Identify the blood parasite species.
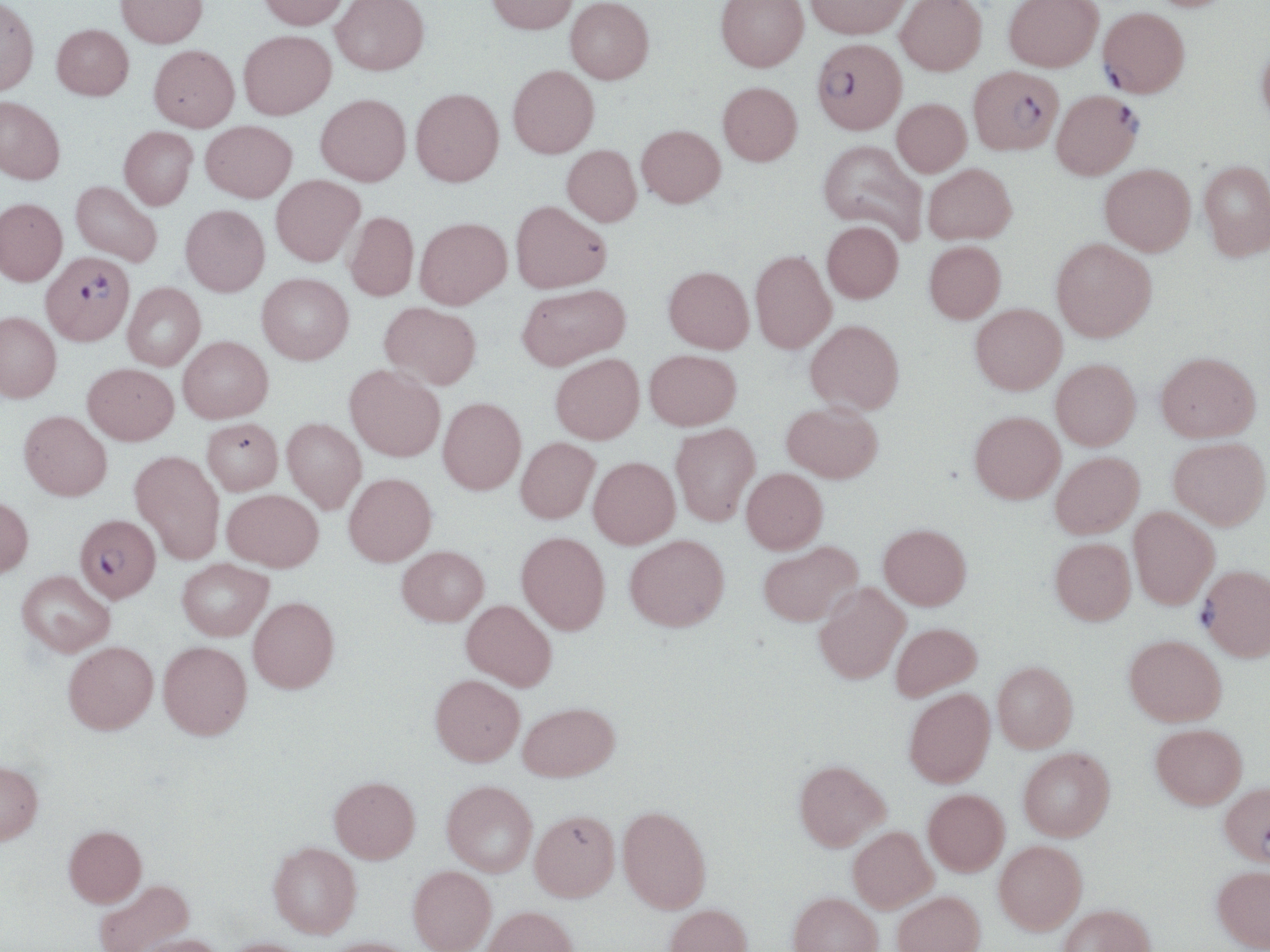

Plasmodium falciparum.

magnification = 1000x
Plasmodium falciparum-infected red blood cell locations = approximate bounding boxes as named x1/y1/x2/y2 corners in pixels: (x1=1098, y1=7, x2=1189, y2=97), (x1=812, y1=38, x2=907, y2=133), (x1=968, y1=66, x2=1064, y2=154), (x1=1052, y1=90, x2=1142, y2=179), (x1=41, y1=251, x2=134, y2=345), (x1=74, y1=514, x2=161, y2=602), (x1=1199, y1=566, x2=1270, y2=660)
preparation = thin blood smear
image size = 1270×952 pixels
uninfected red blood cell locations = approximate bounding boxes as named x1/y1/x2/y2 corners in pixels: (x1=116, y1=0, x2=208, y2=48), (x1=257, y1=0, x2=349, y2=30), (x1=331, y1=0, x2=429, y2=75), (x1=485, y1=0, x2=578, y2=34), (x1=566, y1=0, x2=654, y2=83), (x1=716, y1=0, x2=808, y2=71), (x1=806, y1=0, x2=912, y2=38), (x1=896, y1=0, x2=986, y2=76), (x1=1004, y1=0, x2=1103, y2=71), (x1=0, y1=1, x2=39, y2=96), (x1=51, y1=23, x2=133, y2=100), (x1=239, y1=30, x2=336, y2=119), (x1=1256, y1=36, x2=1270, y2=129), (x1=149, y1=45, x2=239, y2=132), (x1=508, y1=65, x2=599, y2=157), (x1=718, y1=82, x2=802, y2=165), (x1=411, y1=88, x2=504, y2=186), (x1=316, y1=94, x2=411, y2=185), (x1=0, y1=97, x2=65, y2=185), (x1=892, y1=99, x2=971, y2=176), (x1=201, y1=120, x2=296, y2=202), (x1=637, y1=125, x2=725, y2=207), (x1=119, y1=127, x2=197, y2=210), (x1=817, y1=140, x2=928, y2=244), (x1=562, y1=145, x2=641, y2=226), (x1=1199, y1=160, x2=1270, y2=260), (x1=923, y1=163, x2=1016, y2=244), (x1=1100, y1=164, x2=1196, y2=255), (x1=271, y1=175, x2=365, y2=266), (x1=71, y1=181, x2=162, y2=266), (x1=0, y1=198, x2=67, y2=285), (x1=511, y1=201, x2=611, y2=293), (x1=181, y1=205, x2=270, y2=296), (x1=345, y1=211, x2=418, y2=301), (x1=414, y1=217, x2=511, y2=308), (x1=822, y1=221, x2=903, y2=303), (x1=1051, y1=238, x2=1157, y2=341), (x1=924, y1=241, x2=1005, y2=323), (x1=750, y1=250, x2=836, y2=354), (x1=663, y1=266, x2=754, y2=353), (x1=257, y1=272, x2=353, y2=364), (x1=123, y1=283, x2=205, y2=370), (x1=516, y1=284, x2=630, y2=370), (x1=380, y1=302, x2=481, y2=389), (x1=971, y1=304, x2=1066, y2=394), (x1=0, y1=311, x2=61, y2=402), (x1=805, y1=319, x2=904, y2=414), (x1=179, y1=336, x2=273, y2=423), (x1=645, y1=349, x2=741, y2=429), (x1=1156, y1=351, x2=1260, y2=442), (x1=551, y1=353, x2=644, y2=444), (x1=1051, y1=359, x2=1141, y2=449), (x1=83, y1=363, x2=178, y2=445), (x1=345, y1=365, x2=445, y2=461), (x1=438, y1=397, x2=526, y2=494), (x1=782, y1=401, x2=883, y2=483), (x1=19, y1=411, x2=112, y2=500), (x1=970, y1=411, x2=1065, y2=503), (x1=202, y1=418, x2=282, y2=495), (x1=282, y1=418, x2=366, y2=513), (x1=671, y1=423, x2=760, y2=526), (x1=516, y1=437, x2=600, y2=523), (x1=1169, y1=437, x2=1270, y2=529), (x1=130, y1=451, x2=225, y2=564), (x1=1050, y1=452, x2=1144, y2=538), (x1=589, y1=456, x2=680, y2=548), (x1=742, y1=468, x2=828, y2=554), (x1=344, y1=473, x2=436, y2=566), (x1=223, y1=489, x2=323, y2=571), (x1=0, y1=496, x2=33, y2=578), (x1=1129, y1=507, x2=1220, y2=609), (x1=879, y1=524, x2=971, y2=609), (x1=517, y1=531, x2=610, y2=634), (x1=624, y1=534, x2=729, y2=631), (x1=1050, y1=537, x2=1136, y2=624), (x1=758, y1=541, x2=862, y2=626), (x1=397, y1=546, x2=489, y2=625), (x1=178, y1=558, x2=273, y2=640), (x1=17, y1=570, x2=115, y2=657), (x1=815, y1=583, x2=910, y2=683), (x1=248, y1=597, x2=339, y2=693), (x1=461, y1=600, x2=557, y2=690), (x1=891, y1=622, x2=982, y2=701), (x1=1124, y1=635, x2=1227, y2=726), (x1=64, y1=641, x2=158, y2=734), (x1=158, y1=641, x2=252, y2=739), (x1=993, y1=661, x2=1078, y2=751), (x1=431, y1=674, x2=525, y2=765), (x1=904, y1=688, x2=995, y2=787), (x1=518, y1=702, x2=619, y2=781), (x1=1151, y1=724, x2=1246, y2=808), (x1=1018, y1=747, x2=1115, y2=840), (x1=0, y1=760, x2=43, y2=845), (x1=794, y1=760, x2=891, y2=851), (x1=330, y1=776, x2=420, y2=863), (x1=442, y1=780, x2=537, y2=876), (x1=1220, y1=782, x2=1270, y2=866), (x1=923, y1=788, x2=1009, y2=875), (x1=618, y1=806, x2=711, y2=913), (x1=530, y1=810, x2=619, y2=901), (x1=64, y1=825, x2=146, y2=907), (x1=848, y1=826, x2=937, y2=913), (x1=994, y1=840, x2=1087, y2=933), (x1=268, y1=842, x2=361, y2=938), (x1=1212, y1=865, x2=1270, y2=951), (x1=408, y1=866, x2=496, y2=952), (x1=93, y1=879, x2=193, y2=952), (x1=892, y1=891, x2=985, y2=952), (x1=788, y1=892, x2=883, y2=952), (x1=664, y1=903, x2=752, y2=952), (x1=1058, y1=903, x2=1156, y2=952), (x1=482, y1=906, x2=578, y2=952), (x1=132, y1=934, x2=224, y2=952), (x1=323, y1=937, x2=421, y2=952), (x1=219, y1=938, x2=311, y2=952)
stain = May-Grünwald-Giemsa
modality = light microscopy
field of view = one of a larger specimen